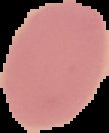
image type = segmented cell region on a black background
preparation = thin blood smear
malaria status = uninfected
image size = 109×133 pixels